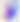
Summary:
  - Magnification: 400x
  - Modality: micrograph
  - Identification: Toxoplasma gondii